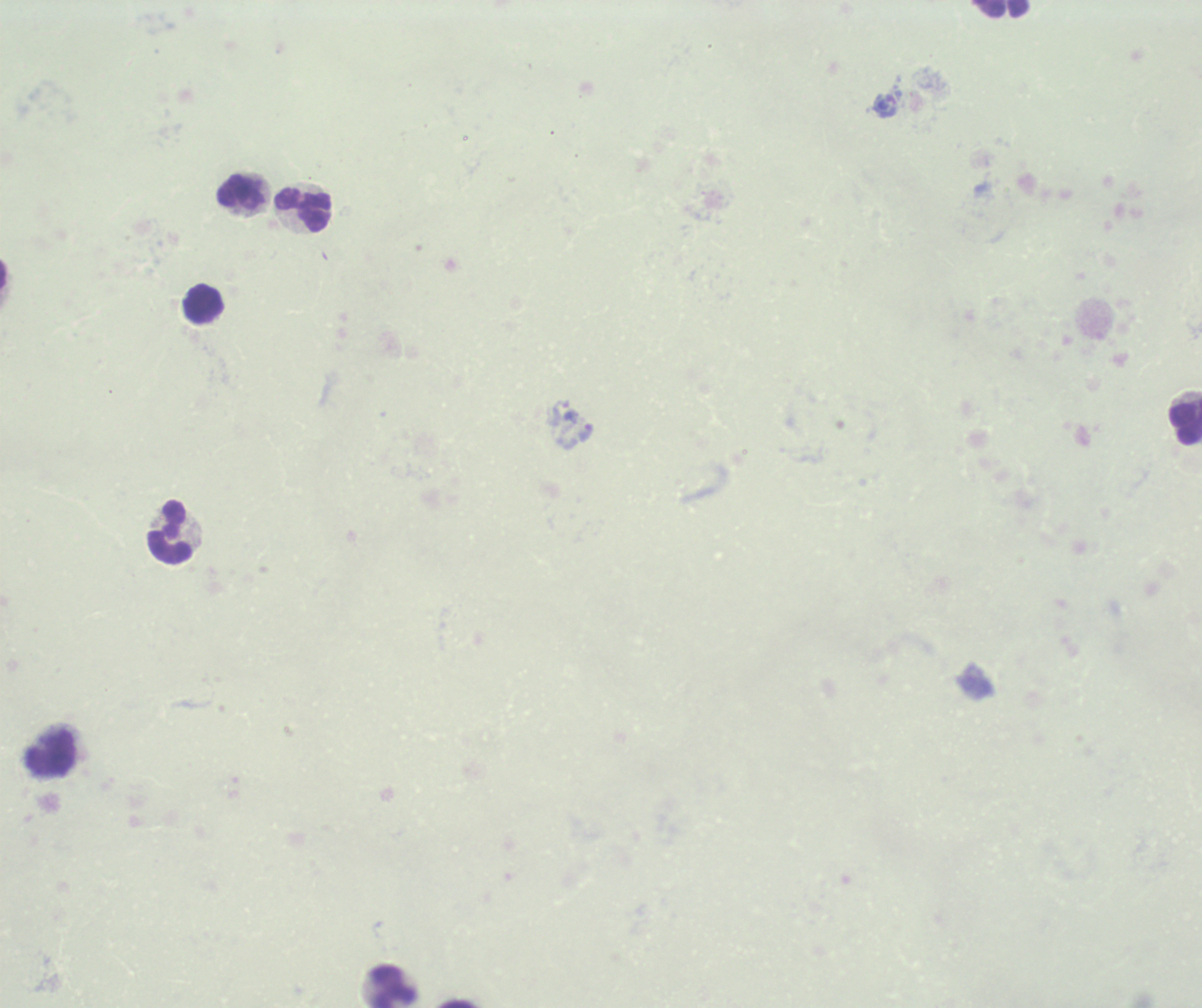
{
  "image_size": "1202×1008 pixels",
  "field_of_view": "single",
  "result": "Plasmodium parasites identified",
  "magnification": "100x",
  "trophozoite_locations": "approximate centers as {x, y} in pixels: {586, 433}",
  "stain": "Romanowsky",
  "context": "previously used in a real diagnosis",
  "leukocyte_locations": "approximate centers as {x, y} in pixels: {1001, 9}, {242, 192}, {303, 209}, {202, 303}, {1184, 419}, {170, 532}, {50, 753}, {390, 986}",
  "preparation": "thick blood smear",
  "background_quality": "poor"
}